Comment on the morphology of the red blood cells.
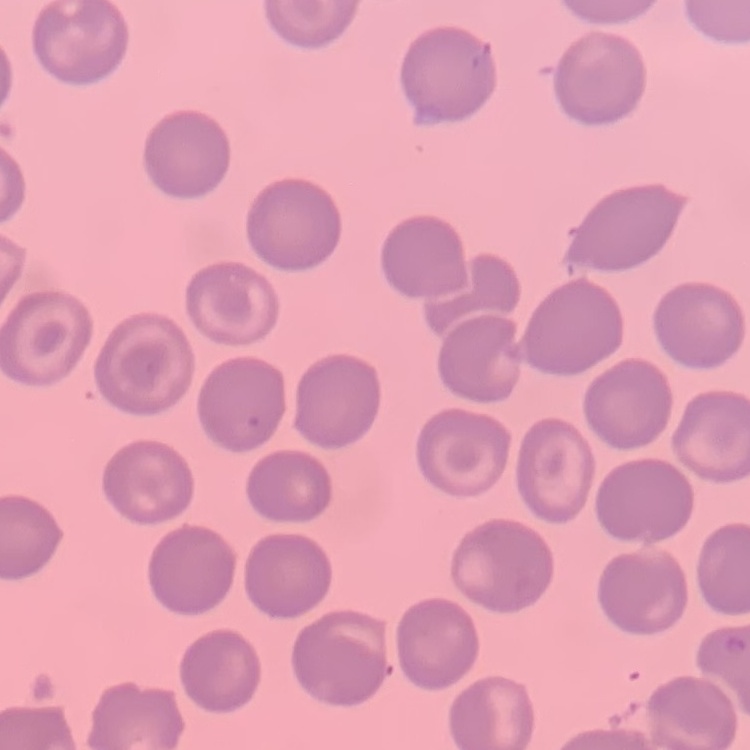

No rouleaux formation.

image type = square crop of a larger photomicrograph
preparation = thin peripheral smear
stain = Field's or Giemsa